Name the parasite shown.
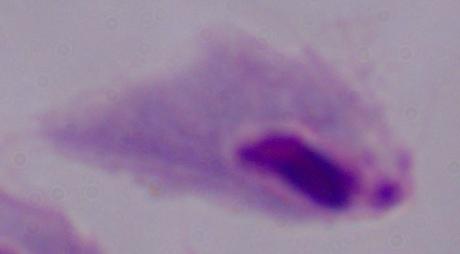

This is a trichomonad.

Photomicrograph. Captured at 1000x magnification.